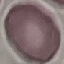

Result: no malaria parasites seen. Giemsa stain. Acquired by smartphone through the microscope eyepiece. Cell patch, automatically extracted from a larger field of view and resized to 64 × 64 pixels. Thin blood smear.